Assess this cell for malaria.
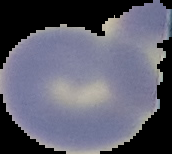
Uninfected.

{
  "image_size": "172×154 pixels",
  "preparation": "thin blood film",
  "image_type": "segmented cell region with the area outside set to black"
}